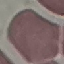 Malaria status: uninfected. Acquired by smartphone through the microscope eyepiece. Thin blood film. Giemsa-stained preparation. Cell patch, automatically extracted from a larger field of view and resized to 64 × 64 pixels.